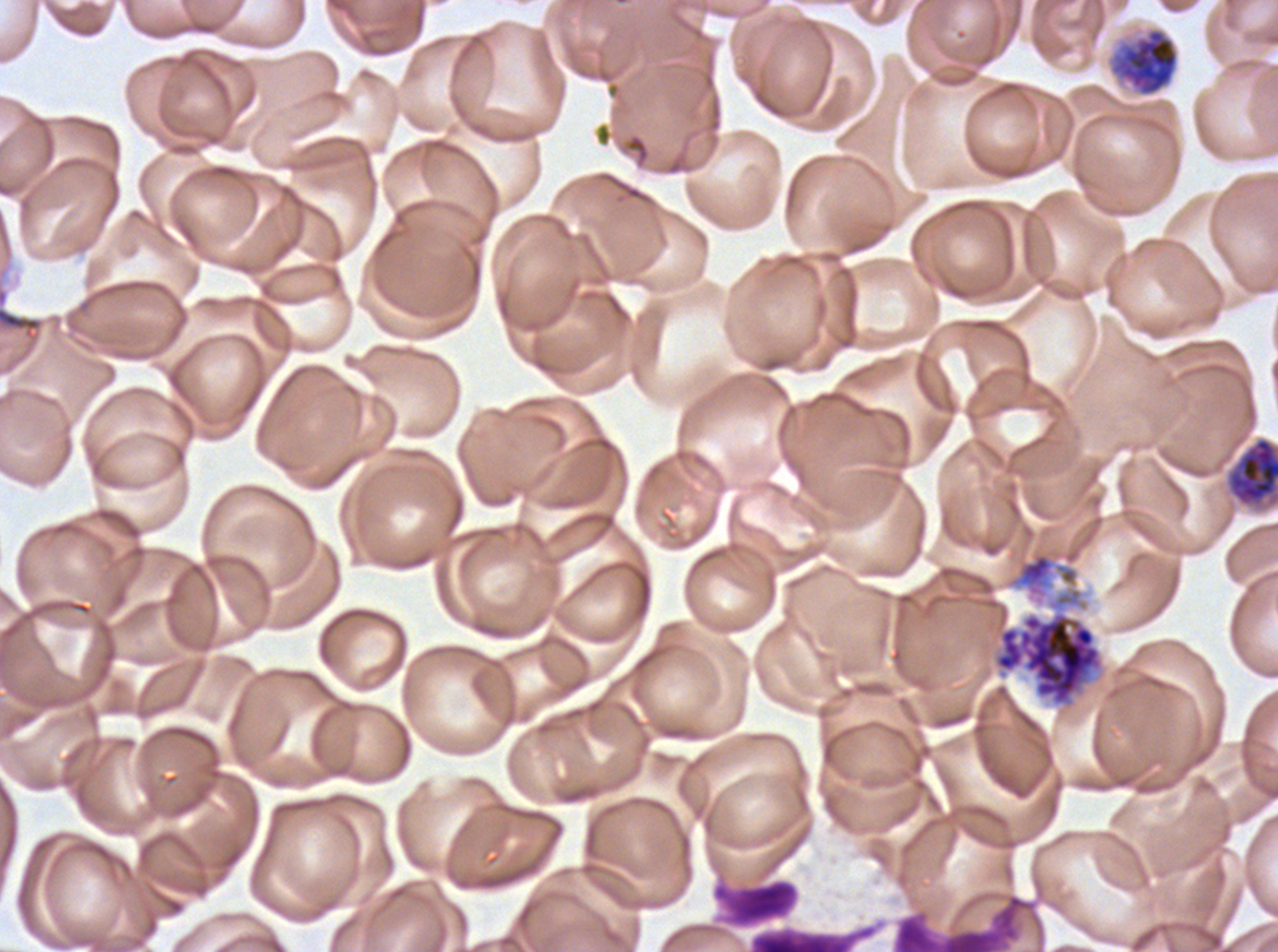
{
  "early_schizont_locations": "approximate bounding boxes as (x1, y1, x2, y2) in pixels: (1109, 27, 1179, 97)",
  "late_schizont_locations": "approximate bounding boxes as (x1, y1, x2, y2) in pixels: (1226, 436, 1277, 507)",
  "stain": "Giemsa",
  "specimen": "P. falciparum from a patient in The Gambia, cultured ex vivo for 24 to 48 hours",
  "image_size": "1278×952 pixels",
  "preparation": "thin blood film",
  "leukocyte_locations": "approximate bounding boxes as (x1, y1, x2, y2) in pixels: (710, 873, 801, 931), (891, 892, 1043, 951)",
  "field_of_view": "one sub-image of a larger composite",
  "segmenter_locations": "approximate bounding boxes as (x1, y1, x2, y2) in pixels: (1007, 514, 1105, 606), (992, 610, 1104, 707)",
  "life_cycle_stages_observed": "early schizont, late schizont, segmenter"
}